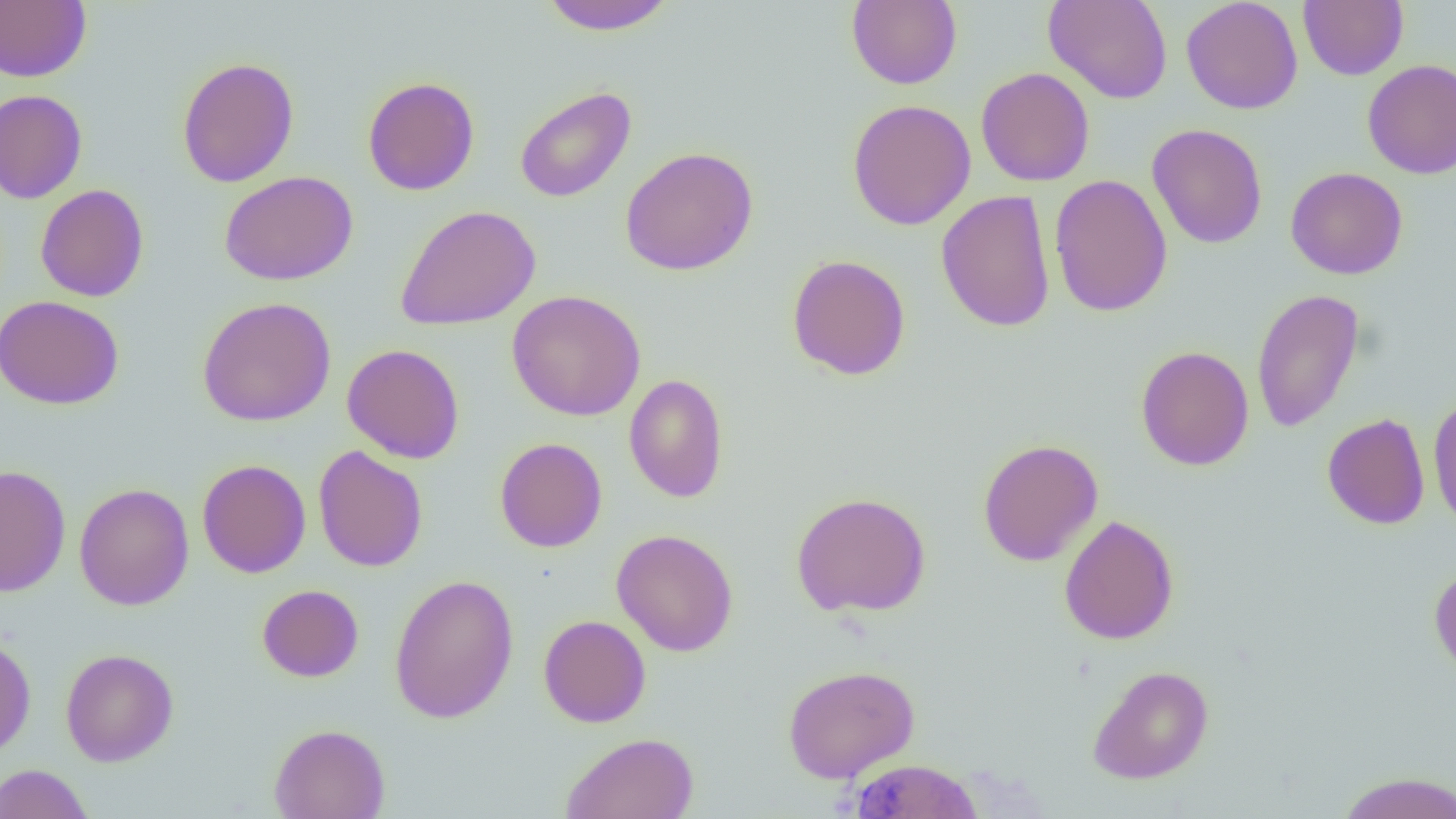
Approximate bounding boxes as [x1, y1, x2, y2] in pixels. Uninfected red blood cell locations: [537, 0, 678, 35], [1043, 0, 1173, 104], [1180, 0, 1303, 114], [1298, 0, 1408, 80], [0, 1, 91, 83], [846, 1, 962, 89], [176, 57, 299, 187], [1362, 59, 1456, 178], [976, 67, 1095, 187], [362, 76, 480, 195], [514, 85, 636, 203], [0, 89, 88, 204], [847, 98, 977, 231], [1146, 123, 1268, 249], [620, 146, 758, 276], [1285, 166, 1408, 280], [219, 171, 358, 285], [1049, 174, 1173, 318], [35, 184, 149, 301], [937, 190, 1056, 332], [393, 204, 541, 331], [786, 253, 911, 381], [1251, 288, 1365, 433], [506, 289, 646, 421], [0, 295, 125, 410], [196, 297, 336, 426], [342, 343, 465, 464], [1136, 346, 1254, 470], [623, 374, 729, 503], [1428, 393, 1456, 533], [1322, 412, 1430, 530], [495, 437, 607, 552], [977, 438, 1103, 566], [313, 446, 428, 572], [196, 459, 311, 578], [1, 464, 71, 597], [74, 483, 194, 611], [791, 491, 931, 617], [1059, 514, 1179, 645], [611, 528, 738, 656], [1429, 565, 1456, 680], [389, 573, 519, 724], [257, 584, 364, 682], [538, 615, 651, 728], [0, 634, 36, 759], [60, 648, 179, 767], [783, 664, 919, 783], [1087, 665, 1214, 784], [269, 723, 390, 819], [561, 732, 699, 819], [848, 758, 984, 818], [0, 763, 94, 819], [1335, 771, 1456, 819]. Slide-level diagnosis: no evidence of blood parasites. Thin blood smear. One field of a larger specimen. 1000x magnification. Image is 1456×819 pixels. Optical microscopy.